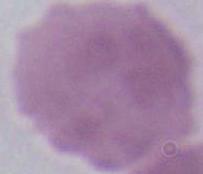
identification = erythrocyte
magnification = 1000x
modality = micrograph